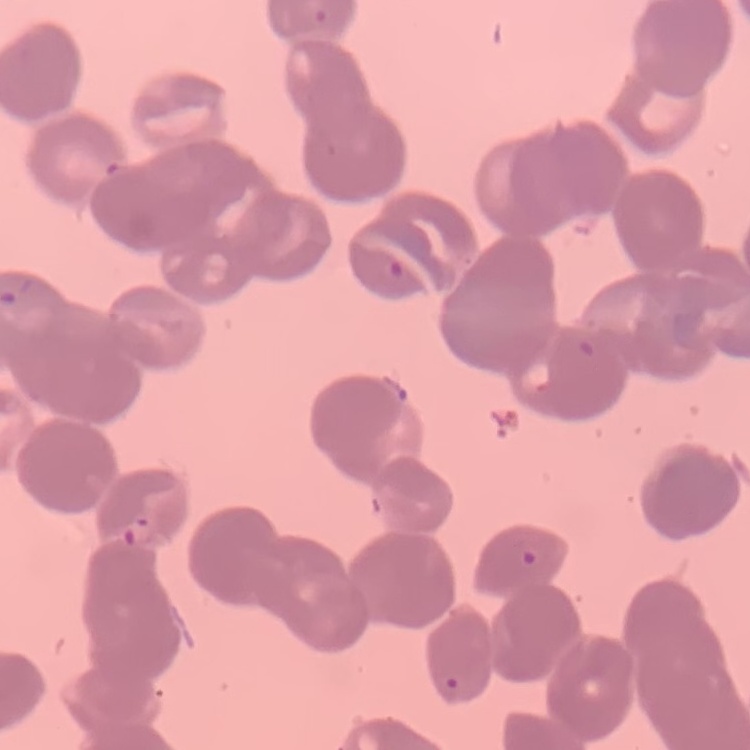

erythrocyte_morphology: rouleaux formation
image_type: square crop of a larger photomicrograph
preparation: thin peripheral smear
stain: Field's or Giemsa